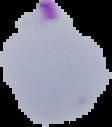

image type = segmented cell region on a black background
preparation = thin blood smear
image size = 112×127 pixels
malaria status = parasitized